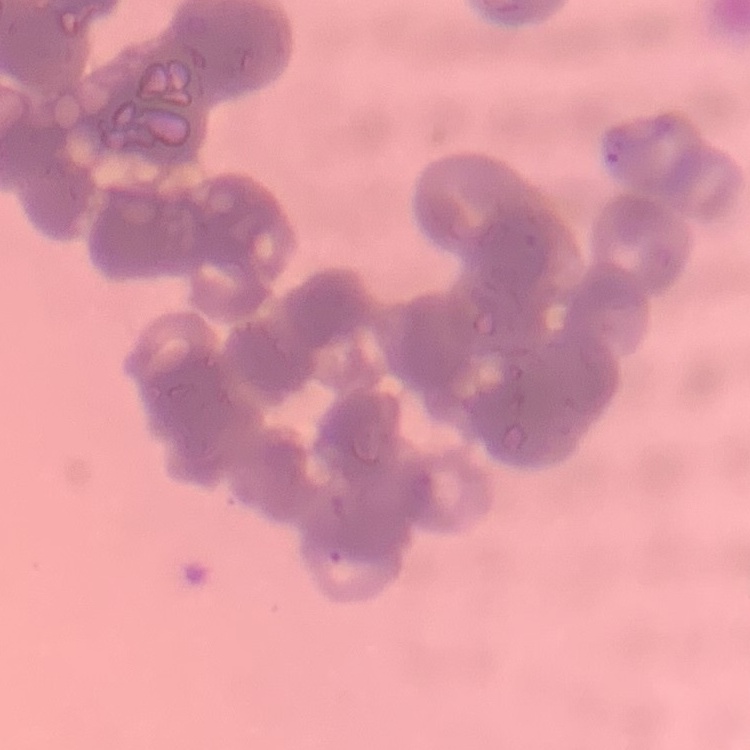

Summary:
  - Erythrocyte morphology: rouleaux formation
  - Preparation: thin peripheral smear
  - Image type: one tile cut from a larger photomicrograph
  - Stain: Field's or Giemsa